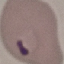
Result: malaria parasites identified. Giemsa-stained preparation. Thin blood film. Cell patch, automatically extracted from a larger field of view and resized to 64 × 64 pixels. Photographed with a smartphone camera at the microscope eyepiece.